Assess this cell for malaria.
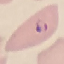

Parasitized.

stain: Giemsa
image_type: automatically extracted cell patch, resized to 64 × 64 pixels
preparation: thin blood film
capture: smartphone camera at the microscope eyepiece